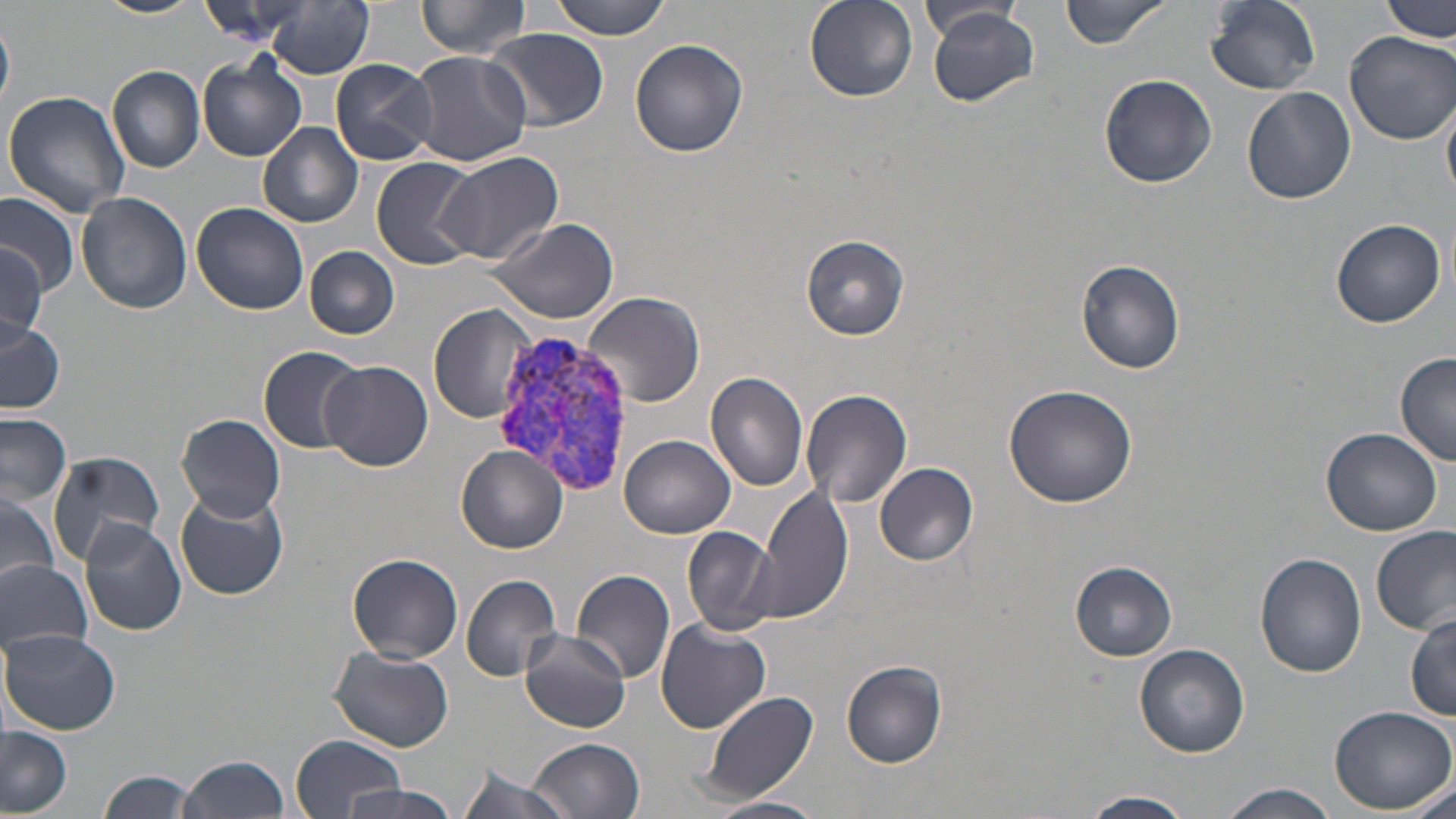
Approximate bounding boxes as named x1/y1/x2/y2 corners in pixels. Uninfected red blood cell locations: (x1=92, y1=0, x2=206, y2=20), (x1=417, y1=0, x2=533, y2=58), (x1=547, y1=0, x2=675, y2=39), (x1=805, y1=0, x2=919, y2=102), (x1=1059, y1=0, x2=1170, y2=48), (x1=1205, y1=0, x2=1322, y2=94), (x1=1381, y1=0, x2=1453, y2=44), (x1=197, y1=1, x2=312, y2=44), (x1=264, y1=2, x2=372, y2=79), (x1=919, y1=4, x2=1023, y2=39), (x1=927, y1=8, x2=1041, y2=106), (x1=0, y1=19, x2=14, y2=109), (x1=485, y1=28, x2=610, y2=128), (x1=1344, y1=30, x2=1456, y2=145), (x1=630, y1=38, x2=749, y2=157), (x1=408, y1=50, x2=530, y2=166), (x1=197, y1=57, x2=305, y2=161), (x1=331, y1=60, x2=438, y2=165), (x1=108, y1=66, x2=205, y2=174), (x1=1100, y1=73, x2=1217, y2=187), (x1=1243, y1=87, x2=1356, y2=204), (x1=3, y1=91, x2=131, y2=218), (x1=1442, y1=92, x2=1456, y2=203), (x1=259, y1=122, x2=363, y2=228), (x1=435, y1=150, x2=565, y2=266), (x1=370, y1=157, x2=479, y2=269), (x1=76, y1=192, x2=191, y2=314), (x1=0, y1=193, x2=78, y2=294), (x1=190, y1=201, x2=309, y2=315), (x1=486, y1=215, x2=620, y2=325), (x1=1329, y1=217, x2=1447, y2=328), (x1=800, y1=233, x2=912, y2=341), (x1=0, y1=244, x2=48, y2=347), (x1=305, y1=246, x2=399, y2=339), (x1=1075, y1=258, x2=1186, y2=374), (x1=586, y1=292, x2=705, y2=406), (x1=428, y1=303, x2=538, y2=425), (x1=0, y1=316, x2=63, y2=414), (x1=258, y1=346, x2=366, y2=453), (x1=1396, y1=352, x2=1456, y2=465), (x1=322, y1=361, x2=432, y2=471), (x1=705, y1=372, x2=810, y2=493), (x1=1003, y1=385, x2=1136, y2=508), (x1=802, y1=388, x2=912, y2=509), (x1=177, y1=412, x2=286, y2=521), (x1=0, y1=414, x2=73, y2=505), (x1=1320, y1=427, x2=1443, y2=535), (x1=621, y1=433, x2=736, y2=539), (x1=457, y1=447, x2=567, y2=553), (x1=48, y1=449, x2=163, y2=565), (x1=875, y1=463, x2=979, y2=565), (x1=758, y1=484, x2=853, y2=626), (x1=174, y1=488, x2=289, y2=602), (x1=0, y1=489, x2=60, y2=595), (x1=79, y1=519, x2=185, y2=635), (x1=683, y1=525, x2=776, y2=636), (x1=1372, y1=526, x2=1456, y2=635), (x1=1255, y1=551, x2=1368, y2=678), (x1=347, y1=552, x2=463, y2=663), (x1=0, y1=558, x2=95, y2=655), (x1=1070, y1=561, x2=1177, y2=660), (x1=571, y1=569, x2=675, y2=684), (x1=461, y1=575, x2=562, y2=681), (x1=1406, y1=612, x2=1456, y2=722), (x1=656, y1=619, x2=773, y2=734), (x1=520, y1=629, x2=629, y2=732), (x1=1, y1=631, x2=120, y2=734), (x1=1135, y1=644, x2=1251, y2=758), (x1=328, y1=646, x2=455, y2=752), (x1=840, y1=659, x2=950, y2=768), (x1=696, y1=690, x2=821, y2=805), (x1=1328, y1=705, x2=1456, y2=815), (x1=0, y1=727, x2=73, y2=817), (x1=290, y1=733, x2=408, y2=818), (x1=527, y1=737, x2=645, y2=819), (x1=177, y1=756, x2=293, y2=819), (x1=455, y1=763, x2=574, y2=819), (x1=98, y1=769, x2=200, y2=819), (x1=1399, y1=778, x2=1454, y2=819), (x1=1213, y1=783, x2=1341, y2=819), (x1=341, y1=785, x2=468, y2=819), (x1=1080, y1=790, x2=1197, y2=818), (x1=709, y1=795, x2=825, y2=819). Plasmodium vivax-infected red blood cell locations: (x1=485, y1=330, x2=641, y2=496). Slide-level diagnosis: Plasmodium vivax. One field of a larger specimen. Light microscopy. Image is 1456×819 pixels. May-Grünwald-Giemsa-stained preparation. Thin blood smear. Captured at 1000x magnification.